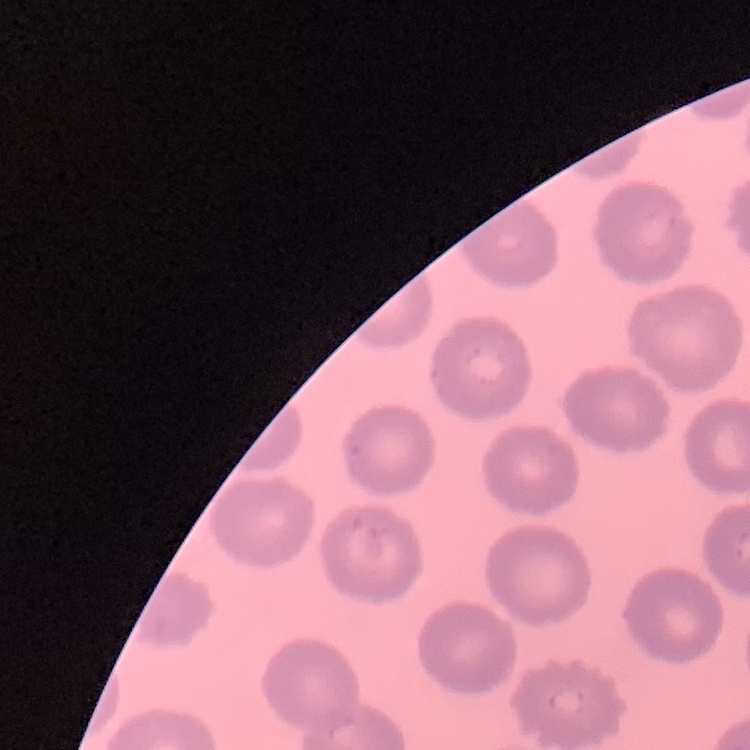
The red blood cells exhibit no rouleaux formation. Stained with either Field's or Giemsa. One tile cut from a larger photomicrograph. Thin peripheral smear.